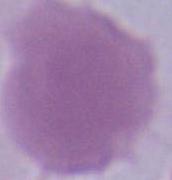

Micrograph. An erythrocyte is seen. 1000x magnification.